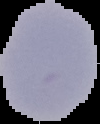
image type = segmented cell region on a black background
malaria status = uninfected
preparation = thin blood film
image size = 100×124 pixels